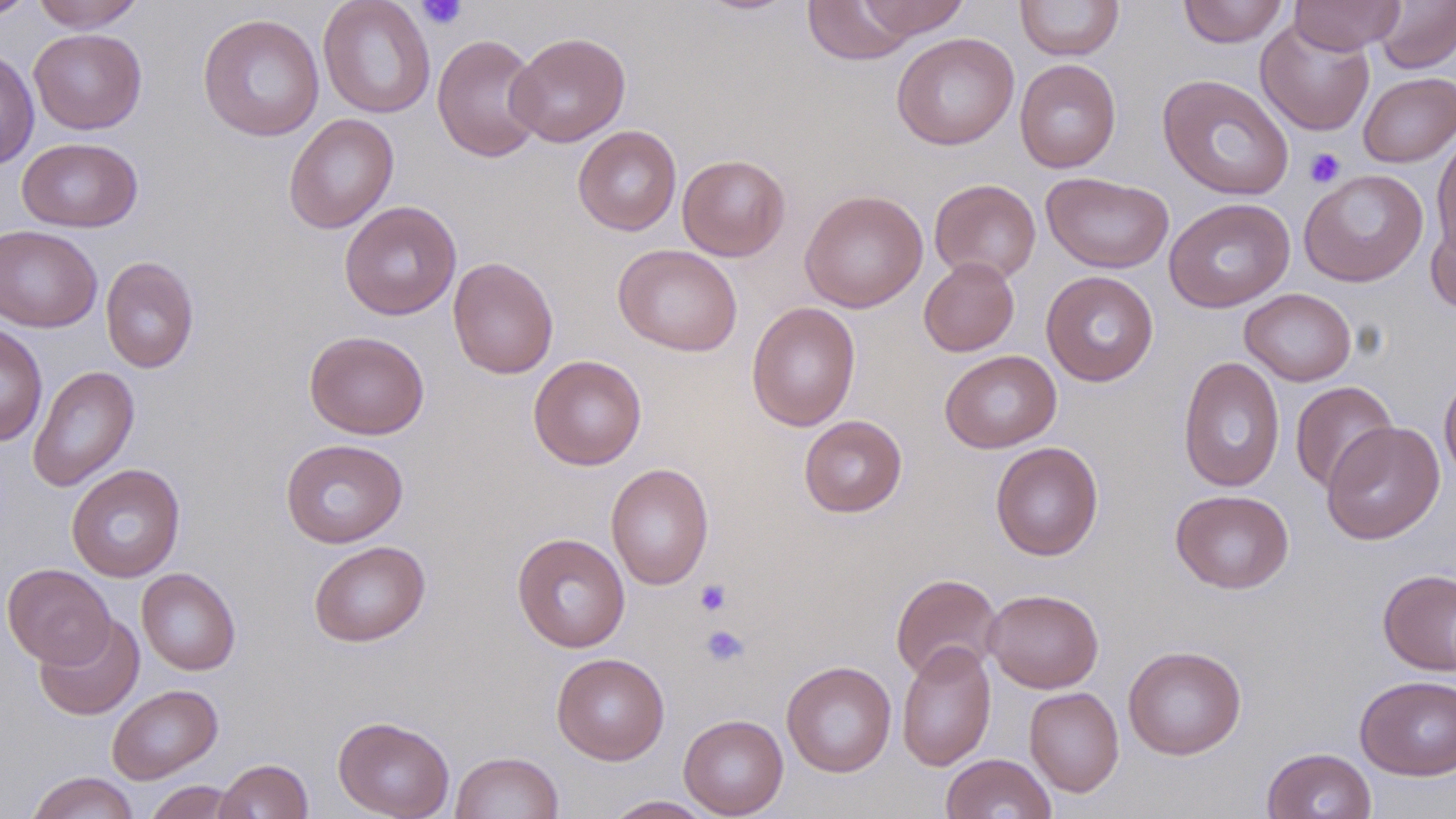
slide-level diagnosis = negative for blood parasites
modality = light microscopy
field of view = single
magnification = 1000x
image size = 1456×819 pixels
stain = May-Grünwald-Giemsa
platelet locations = approximate bounding boxes as (x1, y1, x2, y2) in pixels: (415, 0, 468, 31), (1304, 147, 1346, 188), (695, 579, 732, 616), (699, 624, 751, 668)
uninfected red blood cell locations = approximate bounding boxes as (x1, y1, x2, y2) in pixels: (0, 0, 40, 22), (32, 0, 145, 32), (318, 0, 436, 118), (855, 0, 969, 39), (1015, 0, 1124, 61), (1177, 0, 1289, 48), (1290, 0, 1404, 53), (1374, 0, 1456, 73), (802, 1, 916, 65), (197, 13, 325, 141), (1255, 19, 1375, 136), (29, 28, 147, 134), (506, 31, 631, 147), (891, 32, 1019, 150), (431, 33, 546, 163), (0, 48, 39, 170), (1015, 59, 1121, 173), (1358, 71, 1456, 167), (1157, 74, 1295, 201), (283, 113, 399, 234), (572, 125, 682, 236), (1432, 133, 1456, 255), (16, 137, 143, 232), (677, 154, 791, 261), (1299, 169, 1428, 287), (1042, 172, 1174, 274), (929, 179, 1041, 284), (800, 189, 928, 313), (1164, 197, 1295, 312), (339, 201, 462, 320), (1425, 211, 1456, 315), (0, 226, 102, 332), (613, 243, 743, 356), (100, 256, 199, 373), (447, 257, 558, 379), (919, 257, 1019, 357), (1041, 270, 1159, 387), (1240, 288, 1356, 386), (746, 301, 861, 431), (0, 322, 48, 446), (304, 330, 429, 439), (940, 350, 1062, 453), (528, 355, 646, 470), (1178, 356, 1285, 493), (27, 365, 140, 492), (1439, 370, 1456, 485), (1289, 381, 1399, 494), (799, 415, 907, 518), (1320, 422, 1444, 543), (280, 438, 408, 548), (990, 441, 1103, 561), (66, 463, 186, 582), (606, 463, 714, 591), (1170, 489, 1294, 594), (512, 533, 630, 653), (308, 540, 430, 647), (2, 563, 115, 668), (1378, 567, 1456, 676), (137, 568, 241, 675), (891, 573, 1003, 682), (983, 588, 1103, 693), (34, 614, 145, 720), (896, 641, 997, 771), (1123, 645, 1246, 760), (551, 652, 670, 765), (781, 660, 897, 777), (1355, 674, 1456, 780), (107, 684, 223, 784), (1024, 687, 1124, 796), (678, 714, 789, 818), (333, 716, 455, 819), (1262, 747, 1376, 819), (450, 751, 564, 819), (941, 753, 1056, 819), (215, 758, 313, 818), (25, 771, 140, 819), (144, 780, 247, 819), (603, 795, 717, 818)
preparation = thin blood film